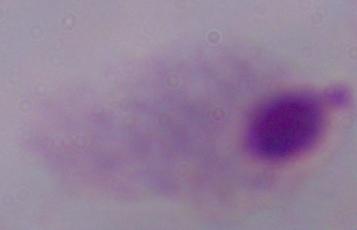
{
  "modality": "photomicrograph",
  "identification": "trichomonad",
  "magnification": "1000x"
}